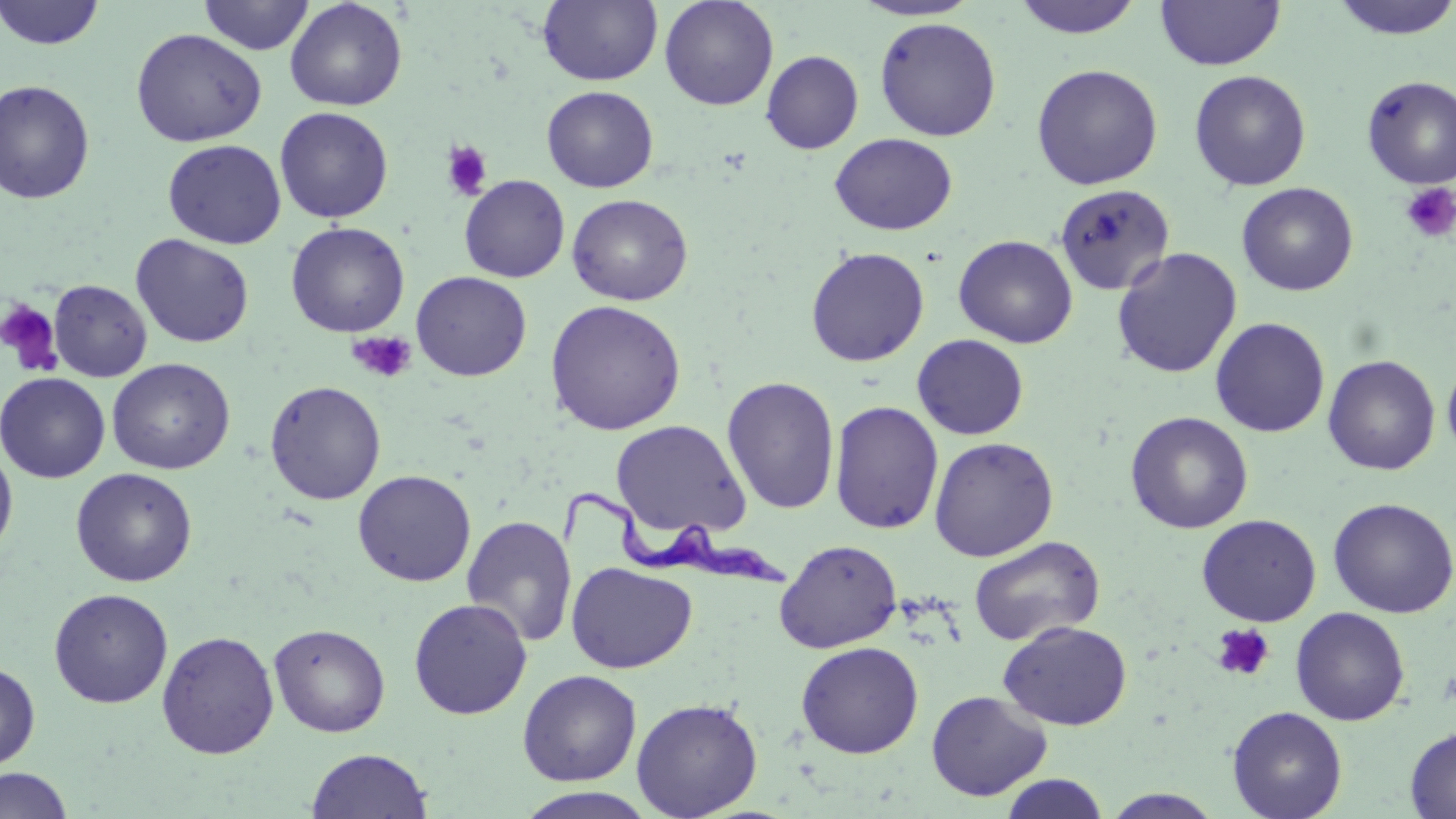

slide-level diagnosis = Trypanosoma brucei
image size = 1456×819 pixels
modality = light microscopy
platelet locations = approximate bounding boxes as named x1/y1/x2/y2 corners in pixels: (x1=441, y1=141, x2=493, y2=201), (x1=1400, y1=181, x2=1456, y2=243), (x1=0, y1=298, x2=62, y2=375), (x1=347, y1=329, x2=417, y2=384), (x1=1210, y1=623, x2=1276, y2=682)
magnification = 1000x
preparation = thin blood film
uninfected red blood cell locations = approximate bounding boxes as named x1/y1/x2/y2 corners in pixels: (x1=0, y1=0, x2=106, y2=50), (x1=198, y1=0, x2=314, y2=55), (x1=285, y1=0, x2=407, y2=111), (x1=538, y1=0, x2=662, y2=86), (x1=659, y1=0, x2=779, y2=111), (x1=850, y1=0, x2=981, y2=22), (x1=1010, y1=0, x2=1146, y2=39), (x1=1156, y1=0, x2=1284, y2=70), (x1=1327, y1=0, x2=1456, y2=41), (x1=874, y1=16, x2=1001, y2=141), (x1=130, y1=28, x2=267, y2=147), (x1=761, y1=50, x2=864, y2=154), (x1=1031, y1=63, x2=1163, y2=190), (x1=1189, y1=70, x2=1311, y2=191), (x1=1361, y1=75, x2=1456, y2=189), (x1=0, y1=79, x2=96, y2=204), (x1=541, y1=85, x2=658, y2=193), (x1=274, y1=106, x2=394, y2=223), (x1=829, y1=133, x2=957, y2=236), (x1=162, y1=139, x2=286, y2=249), (x1=459, y1=174, x2=570, y2=282), (x1=1055, y1=182, x2=1176, y2=296), (x1=1236, y1=182, x2=1358, y2=296), (x1=567, y1=193, x2=693, y2=306), (x1=286, y1=222, x2=410, y2=337), (x1=130, y1=234, x2=255, y2=348), (x1=953, y1=234, x2=1078, y2=348), (x1=805, y1=246, x2=930, y2=367), (x1=1111, y1=247, x2=1242, y2=379), (x1=411, y1=271, x2=532, y2=381), (x1=49, y1=279, x2=152, y2=382), (x1=545, y1=299, x2=685, y2=435), (x1=1210, y1=317, x2=1330, y2=438), (x1=912, y1=334, x2=1029, y2=440), (x1=1442, y1=351, x2=1456, y2=463), (x1=1322, y1=354, x2=1440, y2=475), (x1=107, y1=358, x2=235, y2=474), (x1=0, y1=372, x2=111, y2=483), (x1=722, y1=376, x2=840, y2=514), (x1=264, y1=380, x2=386, y2=505), (x1=829, y1=400, x2=944, y2=534), (x1=1125, y1=411, x2=1253, y2=534), (x1=611, y1=419, x2=751, y2=539), (x1=929, y1=436, x2=1059, y2=562), (x1=0, y1=440, x2=18, y2=563), (x1=70, y1=467, x2=197, y2=587), (x1=352, y1=470, x2=476, y2=587), (x1=1328, y1=497, x2=1456, y2=618), (x1=1196, y1=514, x2=1321, y2=626), (x1=461, y1=515, x2=577, y2=647), (x1=969, y1=536, x2=1105, y2=646), (x1=774, y1=539, x2=902, y2=653), (x1=566, y1=561, x2=698, y2=674), (x1=48, y1=588, x2=173, y2=708), (x1=408, y1=597, x2=532, y2=720), (x1=1290, y1=607, x2=1410, y2=726), (x1=998, y1=620, x2=1132, y2=730), (x1=269, y1=623, x2=390, y2=737), (x1=157, y1=630, x2=279, y2=760), (x1=796, y1=641, x2=923, y2=758), (x1=0, y1=661, x2=40, y2=770), (x1=517, y1=670, x2=641, y2=786), (x1=926, y1=690, x2=1052, y2=801), (x1=631, y1=698, x2=763, y2=818), (x1=1227, y1=705, x2=1347, y2=819), (x1=1405, y1=726, x2=1456, y2=818), (x1=306, y1=748, x2=433, y2=819), (x1=0, y1=768, x2=74, y2=818), (x1=998, y1=773, x2=1111, y2=818), (x1=514, y1=787, x2=659, y2=819), (x1=1101, y1=789, x2=1225, y2=818)
stain = May-Grünwald-Giemsa
field of view = single
Trypanosoma brucei locations = approximate bounding boxes as named x1/y1/x2/y2 corners in pixels: (x1=555, y1=486, x2=797, y2=597)